Name the parasite shown.
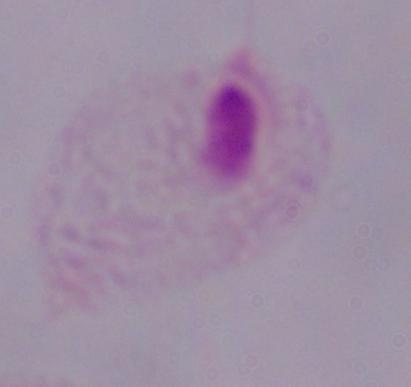

A trichomonad.

Summary:
  - Modality: micrograph
  - Magnification: 1000x